Identify the parasite.
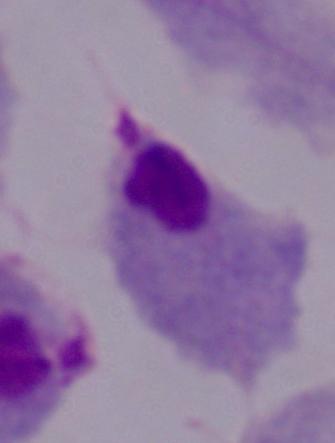
A trichomonad.

Photomicrograph. Captured at 1000x magnification.